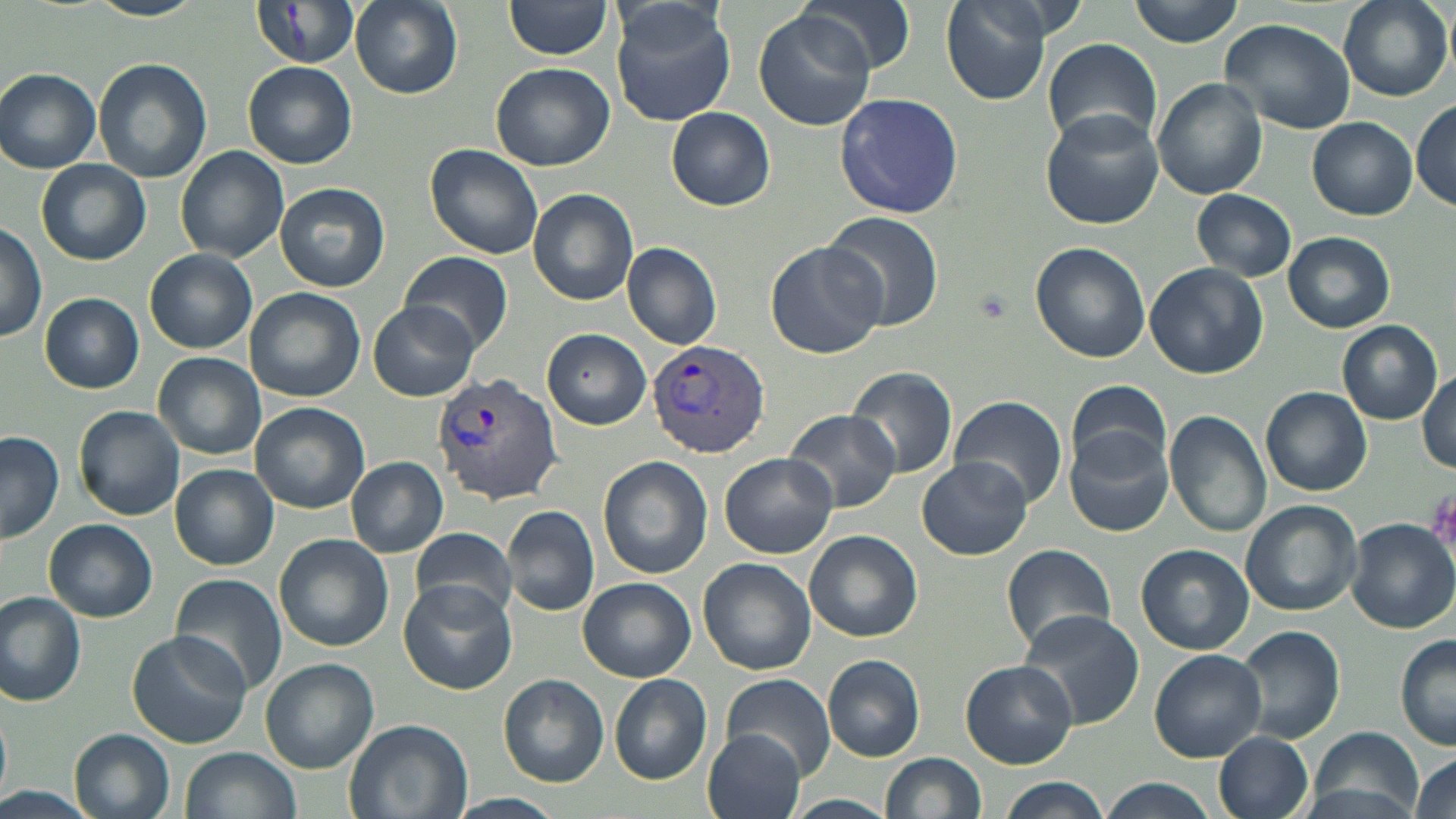
Summary:
  - Coordinate format: approximate bounding boxes as [x1, y1, x2, y2] in pixels
  - Plasmodium vivax-infected red blood cell locations: [646, 339, 773, 458], [435, 374, 562, 505]
  - Uninfected red blood cell locations: [85, 0, 209, 20], [249, 0, 360, 70], [350, 0, 462, 99], [611, 0, 736, 127], [802, 0, 917, 74], [940, 0, 1055, 105], [1128, 0, 1244, 47], [1336, 0, 1451, 103], [503, 2, 611, 61], [752, 7, 876, 133], [1221, 16, 1356, 134], [1043, 38, 1163, 147], [92, 58, 214, 184], [490, 61, 617, 171], [242, 62, 358, 169], [0, 67, 102, 173], [1152, 79, 1266, 201], [835, 94, 963, 219], [1412, 99, 1456, 212], [667, 107, 775, 210], [1039, 109, 1165, 229], [1308, 116, 1416, 219], [425, 142, 544, 260], [175, 146, 289, 261], [36, 158, 151, 266], [274, 182, 390, 292], [528, 188, 639, 305], [1191, 189, 1298, 281], [823, 211, 945, 331], [0, 222, 47, 341], [1283, 232, 1396, 331], [765, 241, 885, 358], [1028, 241, 1152, 364], [622, 242, 723, 350], [146, 249, 257, 353], [401, 250, 512, 353], [1146, 264, 1270, 379], [245, 288, 364, 401], [40, 293, 143, 393], [369, 301, 479, 401], [1336, 321, 1443, 424], [543, 328, 650, 429], [153, 352, 266, 459], [847, 367, 958, 476], [1417, 370, 1454, 471], [1066, 379, 1172, 479], [1260, 387, 1372, 496], [951, 395, 1067, 506], [251, 401, 369, 513], [75, 405, 186, 520], [784, 408, 904, 514], [1166, 409, 1270, 538], [1065, 429, 1174, 538], [0, 431, 64, 544], [720, 454, 838, 558], [599, 456, 714, 579], [347, 457, 447, 558], [918, 458, 1032, 559], [170, 465, 279, 569], [1240, 500, 1363, 615], [502, 505, 601, 617], [44, 519, 158, 621], [1348, 519, 1456, 632], [410, 526, 517, 623], [804, 531, 922, 642], [275, 534, 396, 654], [1001, 543, 1120, 653], [1137, 544, 1253, 654], [698, 557, 816, 675], [171, 574, 288, 694], [398, 578, 517, 694], [579, 578, 696, 681], [0, 591, 87, 706], [1020, 610, 1144, 729], [1236, 625, 1346, 745], [126, 631, 251, 749], [1394, 633, 1456, 752], [1148, 649, 1265, 763], [823, 653, 926, 762], [259, 658, 378, 772], [960, 659, 1077, 768], [722, 672, 835, 779], [499, 674, 608, 786], [609, 674, 713, 784], [0, 707, 12, 803], [345, 717, 471, 819], [70, 728, 176, 819], [701, 728, 807, 819], [1308, 728, 1424, 819], [1214, 731, 1315, 819], [180, 747, 301, 819], [880, 753, 986, 819], [1408, 754, 1456, 819], [1000, 776, 1112, 819], [1099, 778, 1216, 819], [0, 784, 98, 819], [449, 793, 565, 818], [787, 794, 898, 818]
  - Platelet locations: [969, 283, 1018, 327]
  - Slide-level diagnosis: Plasmodium vivax
  - Preparation: thin blood film
  - Magnification: 1000x
  - Image size: 1456×819 pixels
  - Field of view: single
  - Modality: optical microscopy
  - Stain: May-Grünwald-Giemsa